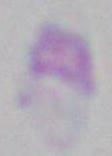

Photomicrograph. Toxoplasma gondii is shown. Captured at 1000x magnification.